Locate and identify every blood parasite.
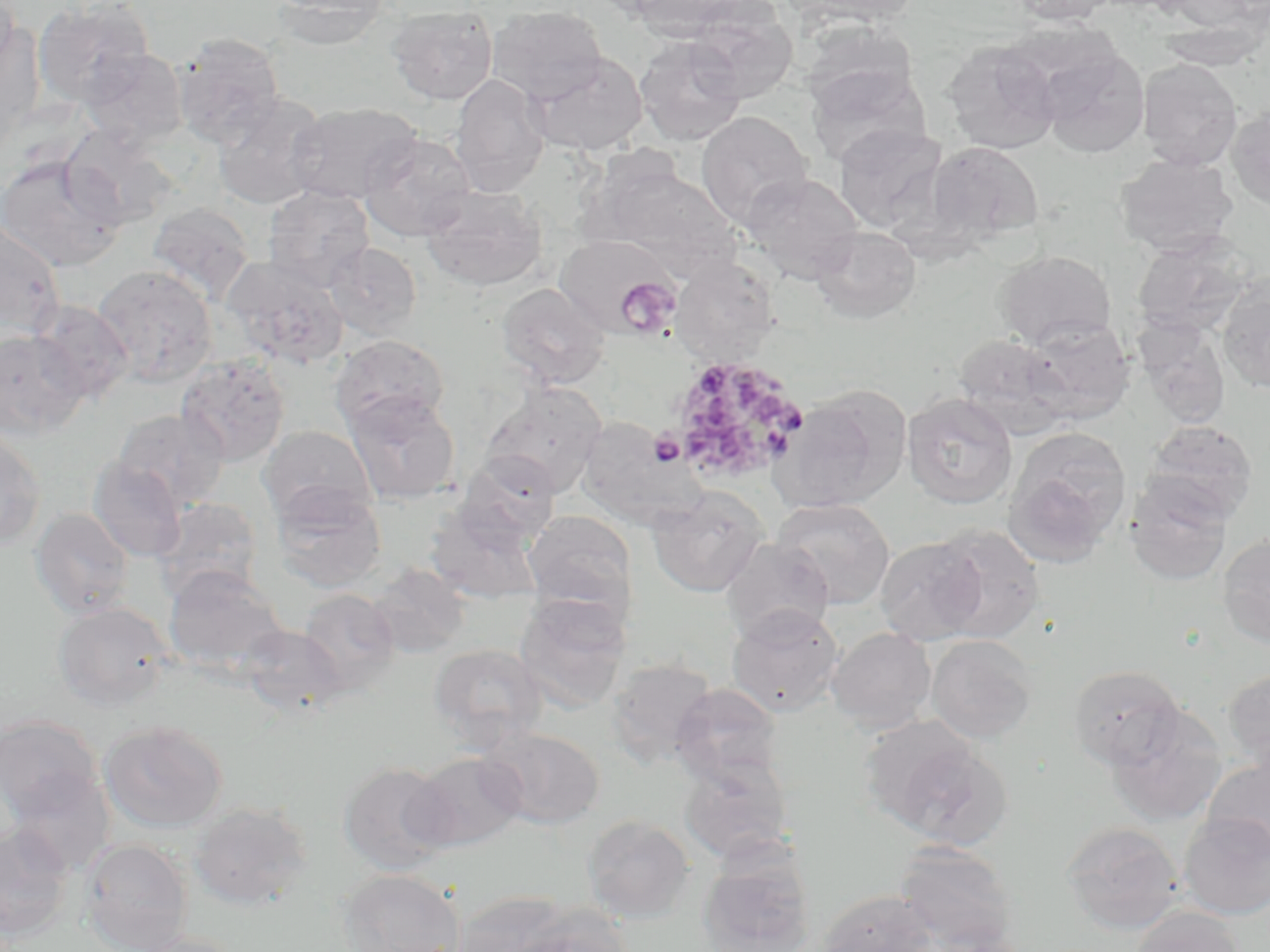
Approximate bounding boxes as [x1, y1, x2, y2] in pixels.
Plasmodium ovale-infected red blood cells: [665, 355, 809, 485].
No Plasmodium falciparum, Plasmodium malariae, Plasmodium vivax, Babesia divergens, or Trypanosoma brucei observed.

Summary:
  - Platelet locations: [614, 276, 682, 339], [649, 432, 686, 466]
  - Uninfected red blood cell locations: [0, 0, 21, 75], [267, 0, 392, 49], [627, 0, 751, 39], [791, 0, 916, 28], [1011, 0, 1119, 25], [1157, 0, 1266, 34], [33, 1, 156, 107], [386, 4, 498, 105], [685, 4, 799, 102], [486, 5, 609, 104], [0, 22, 45, 149], [800, 22, 918, 117], [1155, 22, 1267, 71], [173, 31, 285, 148], [634, 35, 747, 146], [943, 39, 1061, 154], [1037, 44, 1150, 159], [80, 48, 189, 148], [527, 52, 648, 156], [1137, 59, 1243, 171], [804, 62, 931, 169], [449, 73, 550, 196], [212, 92, 329, 210], [285, 101, 422, 205], [1225, 108, 1270, 211], [696, 111, 813, 229], [833, 123, 947, 234], [59, 125, 181, 229], [358, 132, 477, 242], [926, 141, 1044, 247], [1114, 153, 1239, 256], [0, 155, 126, 272], [587, 161, 741, 277], [740, 172, 865, 285], [420, 185, 549, 292], [263, 186, 375, 291], [146, 202, 254, 305], [0, 218, 66, 338], [810, 225, 922, 324], [1131, 232, 1255, 337], [554, 234, 676, 334], [323, 241, 422, 341], [995, 249, 1117, 350], [222, 255, 349, 370], [670, 257, 780, 364], [92, 264, 218, 387], [1217, 273, 1270, 397], [495, 282, 612, 389], [32, 300, 133, 403], [1022, 318, 1136, 424], [1132, 318, 1232, 429], [0, 328, 89, 438], [330, 334, 450, 432], [952, 335, 1074, 440], [175, 354, 291, 466], [481, 381, 608, 497], [774, 385, 911, 513], [344, 392, 460, 504], [902, 392, 1018, 509], [112, 408, 230, 511], [577, 420, 703, 531], [1142, 420, 1258, 526], [258, 425, 377, 524], [0, 426, 47, 551], [1004, 427, 1132, 563], [457, 453, 560, 546], [88, 457, 188, 562], [1125, 474, 1233, 586], [270, 485, 387, 593], [647, 486, 769, 597], [771, 497, 896, 610], [152, 498, 263, 603], [425, 504, 544, 605], [29, 507, 135, 620], [523, 510, 636, 615], [931, 525, 1045, 643], [1217, 532, 1270, 648], [874, 536, 989, 644], [720, 537, 834, 643], [368, 564, 471, 659], [163, 565, 288, 675], [296, 588, 400, 695], [514, 593, 630, 713], [51, 601, 176, 710], [726, 604, 844, 717], [238, 623, 348, 718], [827, 627, 937, 733], [925, 634, 1039, 744], [427, 643, 548, 749], [605, 657, 719, 769], [1067, 664, 1185, 770], [1223, 667, 1270, 773], [670, 683, 783, 786], [1103, 706, 1226, 827], [0, 714, 104, 823], [99, 720, 228, 834], [867, 722, 1010, 850], [481, 726, 605, 830], [408, 752, 526, 851], [677, 755, 794, 865], [1202, 757, 1270, 860], [338, 760, 454, 876], [6, 770, 115, 874], [190, 802, 312, 910], [1178, 812, 1270, 919], [582, 814, 695, 922], [1060, 820, 1185, 934], [0, 825, 75, 940], [81, 838, 194, 952], [895, 842, 1020, 952], [696, 848, 816, 952], [336, 868, 466, 952], [451, 889, 576, 952], [817, 890, 939, 952], [514, 906, 634, 952], [1129, 906, 1245, 952], [128, 932, 248, 952]
  - Slide-level diagnosis: Plasmodium ovale
  - Preparation: thin blood smear
  - Modality: light microscopy
  - Image size: 1270×952 pixels
  - Magnification: 1000x
  - Field of view: one of a larger specimen
  - Stain: May-Grünwald-Giemsa